Locate every uninfected red blood cell.
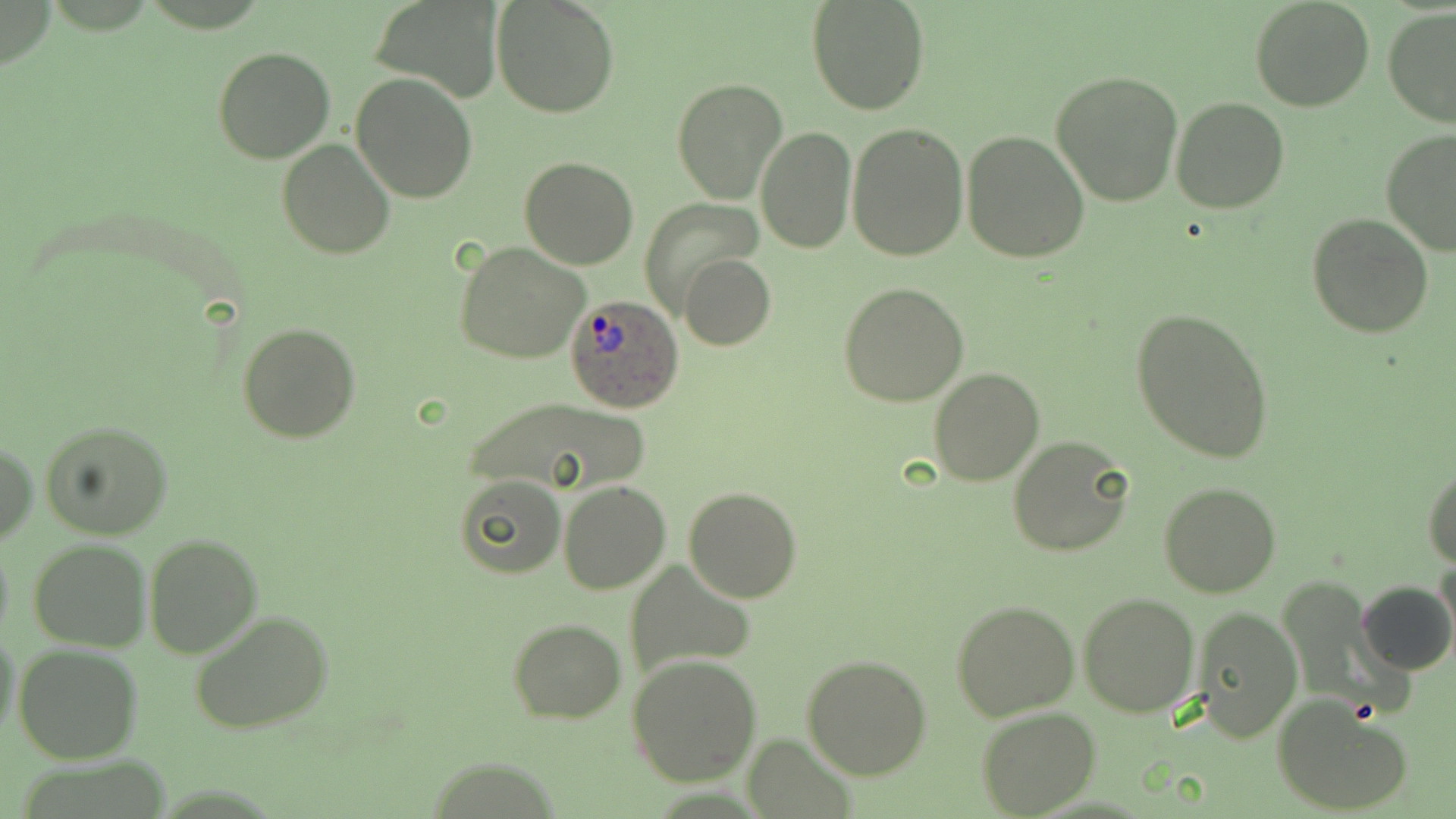
Approximate bounding boxes as (x1, y1, x2, y2) in pixels.
Uninfected red blood cells: (371, 0, 504, 103), (491, 0, 621, 118), (806, 0, 931, 116), (1249, 0, 1376, 113), (1382, 8, 1456, 127), (213, 47, 336, 164), (1050, 71, 1184, 209), (350, 73, 479, 204), (671, 77, 788, 203), (1171, 97, 1290, 215), (845, 121, 970, 262), (756, 127, 857, 253), (961, 130, 1090, 264), (1381, 131, 1455, 256), (277, 139, 395, 259), (518, 157, 639, 270), (639, 198, 761, 314), (1306, 214, 1433, 337), (454, 242, 590, 365), (679, 254, 776, 352), (837, 282, 970, 407), (1131, 305, 1276, 461), (237, 321, 362, 444), (928, 367, 1045, 486), (464, 397, 644, 495), (38, 418, 175, 539), (1008, 434, 1134, 556), (1, 439, 36, 545), (1424, 466, 1456, 569), (452, 473, 565, 580), (558, 481, 670, 595), (1158, 481, 1282, 598), (683, 487, 802, 602), (144, 533, 264, 659), (0, 535, 14, 650), (28, 539, 150, 652), (1434, 558, 1455, 658), (626, 561, 758, 677), (1274, 576, 1402, 716), (1354, 580, 1454, 677), (1078, 592, 1199, 716), (950, 600, 1078, 720), (1193, 607, 1302, 741), (188, 609, 336, 737), (508, 618, 627, 724), (1, 628, 22, 745), (12, 644, 143, 765), (801, 651, 932, 779), (626, 654, 762, 786), (1272, 697, 1414, 817), (977, 708, 1101, 818), (745, 734, 856, 819).

Plasmodium ovale-infected red blood cell locations: (566, 292, 685, 412). Slide-level diagnosis: Plasmodium ovale. May-Grünwald-Giemsa-stained preparation. Thin blood film. One field of a larger specimen. Image is 1456×819 pixels. 1000x magnification. Light microscopy.